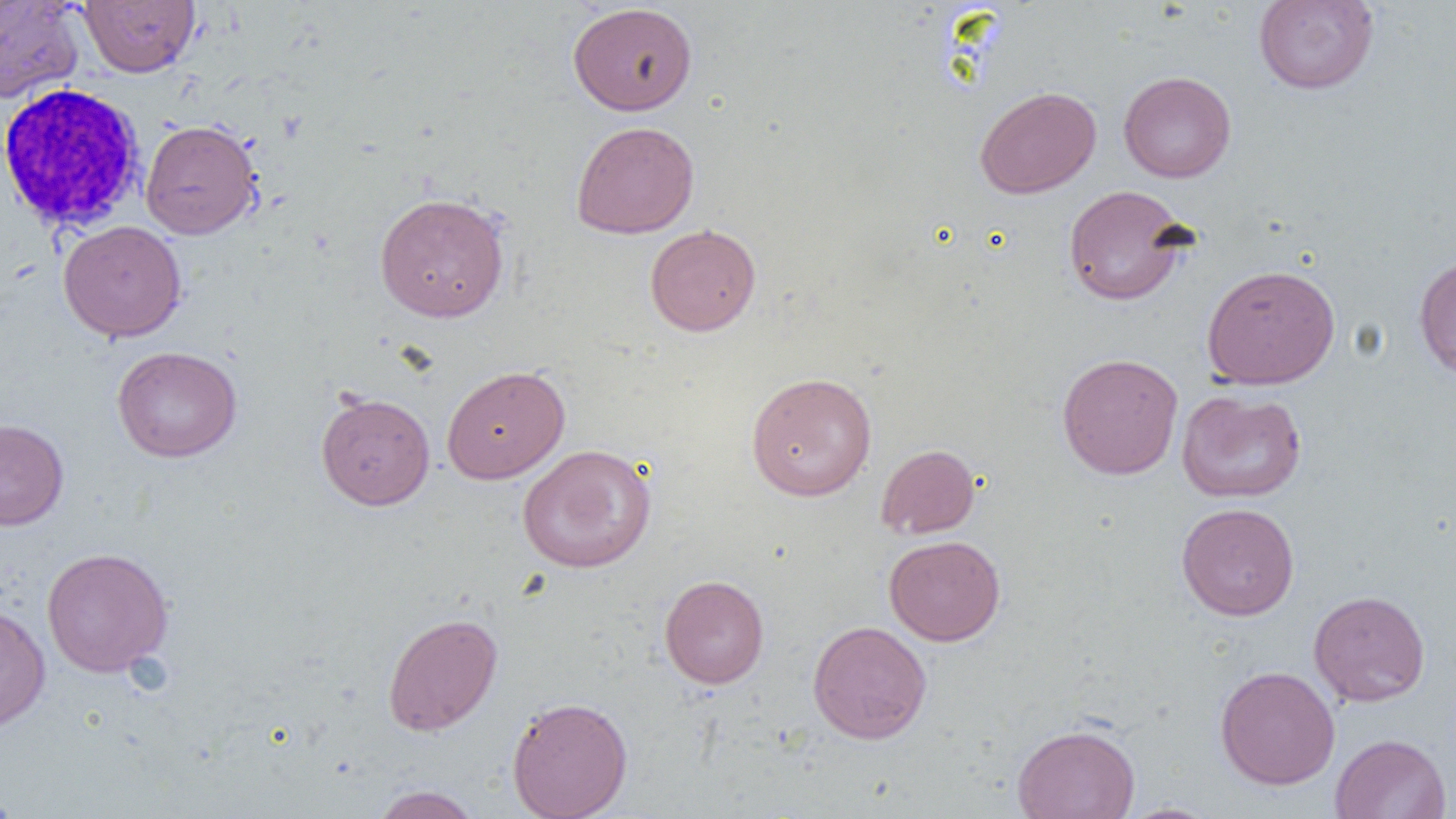
Approximate bounding boxes as [x1, y1, x2, y2] in pixels. Uninfected red blood cell locations: [1253, 0, 1380, 95], [0, 1, 84, 105], [79, 1, 200, 77], [568, 2, 698, 115], [1118, 71, 1236, 183], [974, 85, 1101, 199], [140, 119, 262, 240], [571, 120, 700, 239], [1063, 185, 1192, 306], [373, 192, 510, 323], [58, 220, 187, 342], [645, 223, 761, 335], [1413, 254, 1456, 380], [1201, 263, 1340, 390], [112, 346, 242, 462], [1056, 352, 1184, 479], [441, 365, 570, 484], [745, 371, 877, 501], [1176, 389, 1307, 503], [316, 391, 435, 510], [0, 419, 69, 530], [876, 443, 980, 539], [517, 444, 657, 573], [1176, 502, 1299, 621], [884, 535, 1005, 645], [41, 547, 174, 677], [659, 574, 769, 689], [1308, 589, 1430, 707], [0, 603, 51, 733], [382, 612, 503, 736], [807, 620, 932, 744], [1215, 665, 1340, 790], [506, 695, 633, 818], [1011, 723, 1141, 819], [1331, 733, 1451, 819], [0, 785, 22, 818], [369, 785, 482, 819], [1116, 802, 1224, 819]. White blood cell locations: [0, 82, 147, 235]. Slide-level diagnosis: negative for blood parasites. Thin blood film. Image is 1456×819 pixels. Optical microscopy. 1000x magnification. Single field of view.